Give the preparation type.
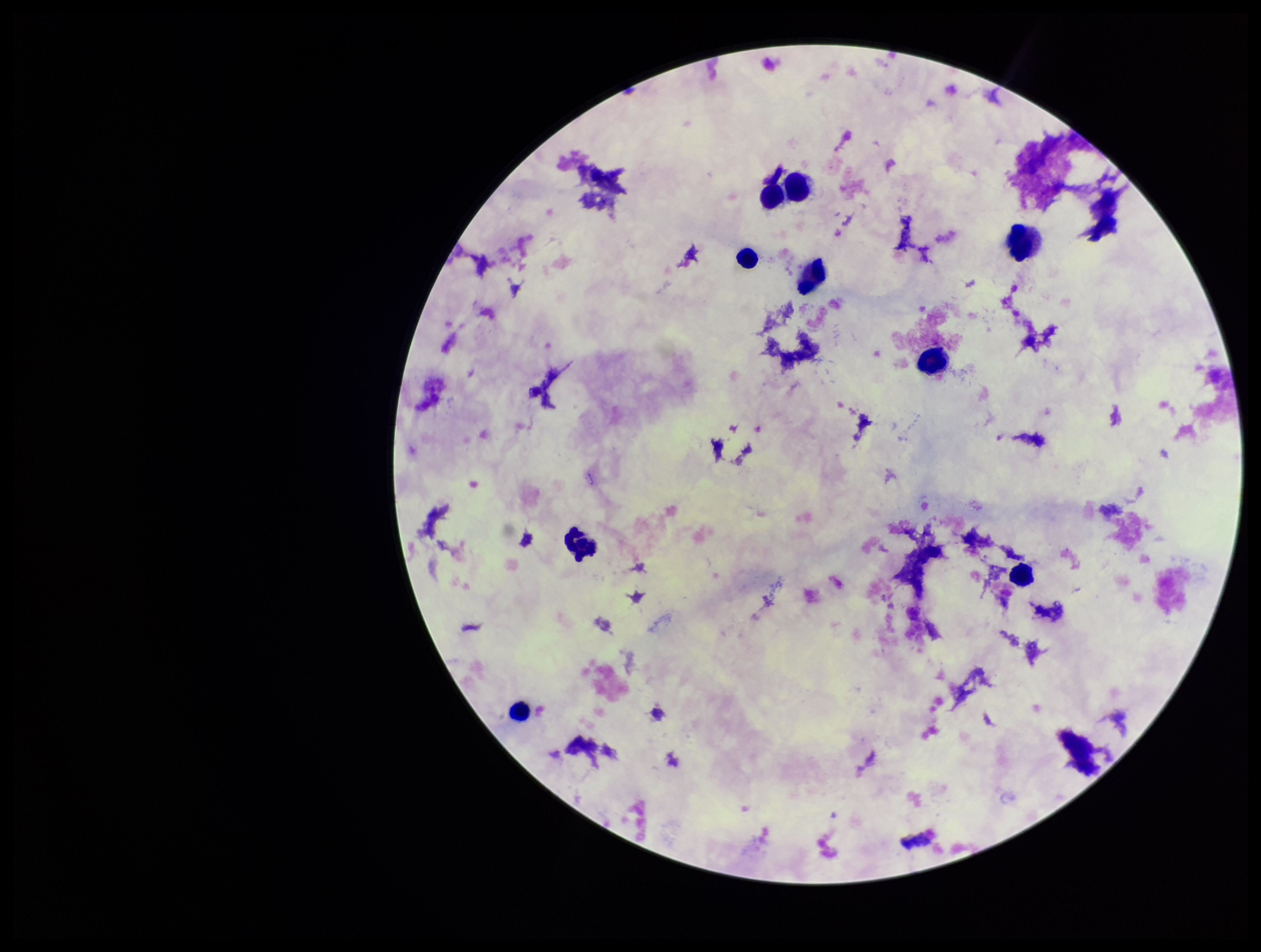
It is a thick blood smear.

{
  "stain": "Giemsa",
  "leukocyte_count": 9,
  "capture": "smartphone photograph through the microscope eyepiece",
  "parasite_count": 0,
  "field_of_view": "one from this slide",
  "plasmodium_parasites": "none detected",
  "image_size": "1261×952 pixels",
  "patient_malaria_status": "negative"
}